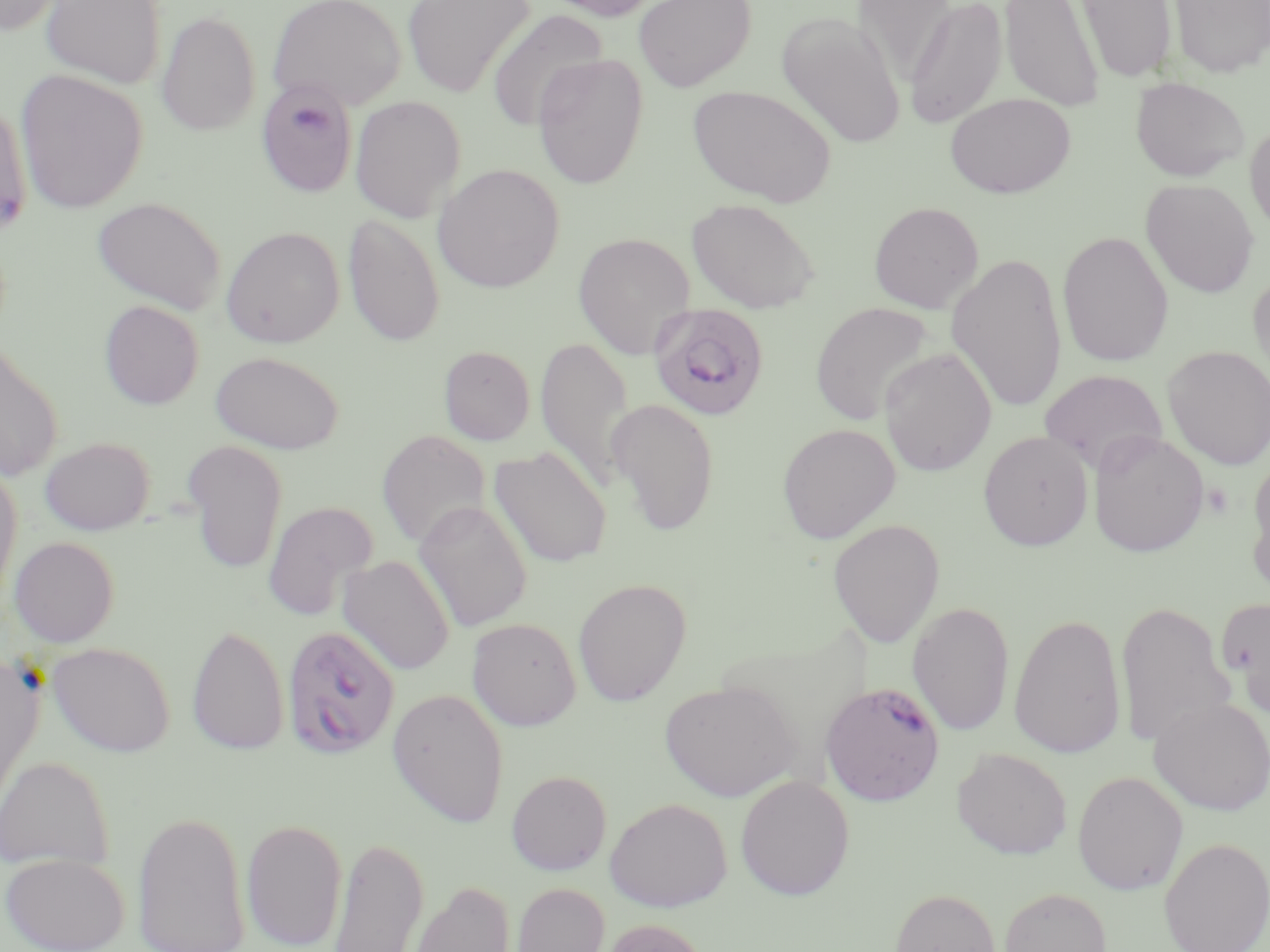 Approximate bounding boxes as (x1,y1)-(x2,y2) corner pairs in pixels. Uninfected red blood cell locations: (0,0)-(71,36), (40,0)-(167,88), (268,0)-(406,111), (403,0)-(535,98), (539,0)-(664,21), (633,0)-(757,92), (853,0)-(957,85), (1000,0)-(1104,112), (1076,0)-(1177,83), (1169,0)-(1270,78), (903,1)-(1008,129), (487,9)-(608,132), (156,11)-(261,136), (777,13)-(905,149), (532,54)-(648,188), (15,70)-(147,214), (1131,76)-(1249,182), (254,80)-(358,198), (688,85)-(836,207), (945,92)-(1076,198), (350,96)-(466,222), (0,99)-(32,238), (1245,120)-(1270,239), (433,163)-(565,293), (1141,179)-(1259,298), (92,196)-(227,314), (686,197)-(822,313), (868,201)-(984,313), (343,213)-(445,347), (221,226)-(345,348), (1057,231)-(1174,367), (573,232)-(696,358), (947,250)-(1068,414), (1247,271)-(1270,392), (99,300)-(204,409), (810,302)-(936,425), (535,336)-(636,490), (0,339)-(63,482), (439,345)-(536,445), (1162,346)-(1270,470), (880,347)-(997,476), (210,350)-(345,454), (1039,369)-(1167,474), (607,398)-(721,536), (776,423)-(900,544), (376,429)-(491,549), (1087,429)-(1209,557), (978,430)-(1094,550), (40,436)-(155,535), (180,440)-(288,575), (489,446)-(612,568), (1247,458)-(1270,593), (0,464)-(22,607), (263,500)-(378,621), (414,500)-(533,632), (827,518)-(945,647), (9,536)-(119,647), (337,555)-(456,675), (573,577)-(691,707), (1220,597)-(1270,717), (1115,599)-(1233,749), (907,601)-(1015,736), (1008,611)-(1127,759), (466,617)-(582,730), (187,624)-(289,757), (48,641)-(175,757), (0,653)-(45,825), (660,680)-(801,802), (387,688)-(510,828), (1149,695)-(1270,816), (952,748)-(1072,859), (0,755)-(115,872), (506,770)-(612,875), (1071,770)-(1188,895), (734,774)-(855,900), (604,797)-(733,912), (132,808)-(250,952), (241,817)-(348,951), (328,833)-(429,951), (1159,837)-(1270,952), (1,851)-(130,952), (406,880)-(516,952), (511,882)-(610,952), (999,886)-(1112,952), (889,887)-(1001,952), (596,917)-(711,952). Plasmodium falciparum-infected red blood cell locations: (648,302)-(770,422), (281,625)-(401,759), (288,632)-(399,756), (820,681)-(945,805). Slide-level diagnosis: Plasmodium falciparum. Captured at 1000x magnification. Optical microscopy. Single field of view. Image is 1270×952 pixels. May-Grünwald-Giemsa stain. Thin blood smear.